Classify this cell by malaria status.
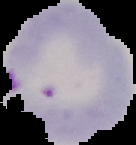

Parasitized.

Image is 136×145 pixels. Segmented cell region on a black background. From a thin blood smear.